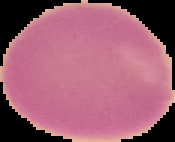

malaria_status: uninfected
image_type: cell region segmented out of the field of view; surrounding area masked to black
image_size: 175×142 pixels
preparation: thin blood film